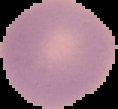
Summary:
  - Result: no Plasmodium parasites detected
  - Image size: 118×109 pixels
  - Image type: cell region segmented out of the field of view; surrounding area masked to black
  - Preparation: thin blood smear